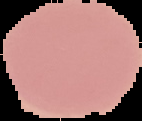
preparation = thin blood smear
image type = segmented cell region on a black background
result = negative for Plasmodium parasites
image size = 142×121 pixels